Classify this cell by malaria status.
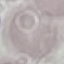
It is uninfected.

Summary:
  - Preparation: thin smear
  - Image type: automatically extracted cell patch, resized to 64 × 64 pixels
  - Stain: Giemsa
  - Capture: smartphone camera at the microscope eyepiece